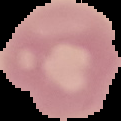

From a thin blood smear. Result: negative for malaria parasites. Image is 121×121 pixels. Segmented cell region on a black background.